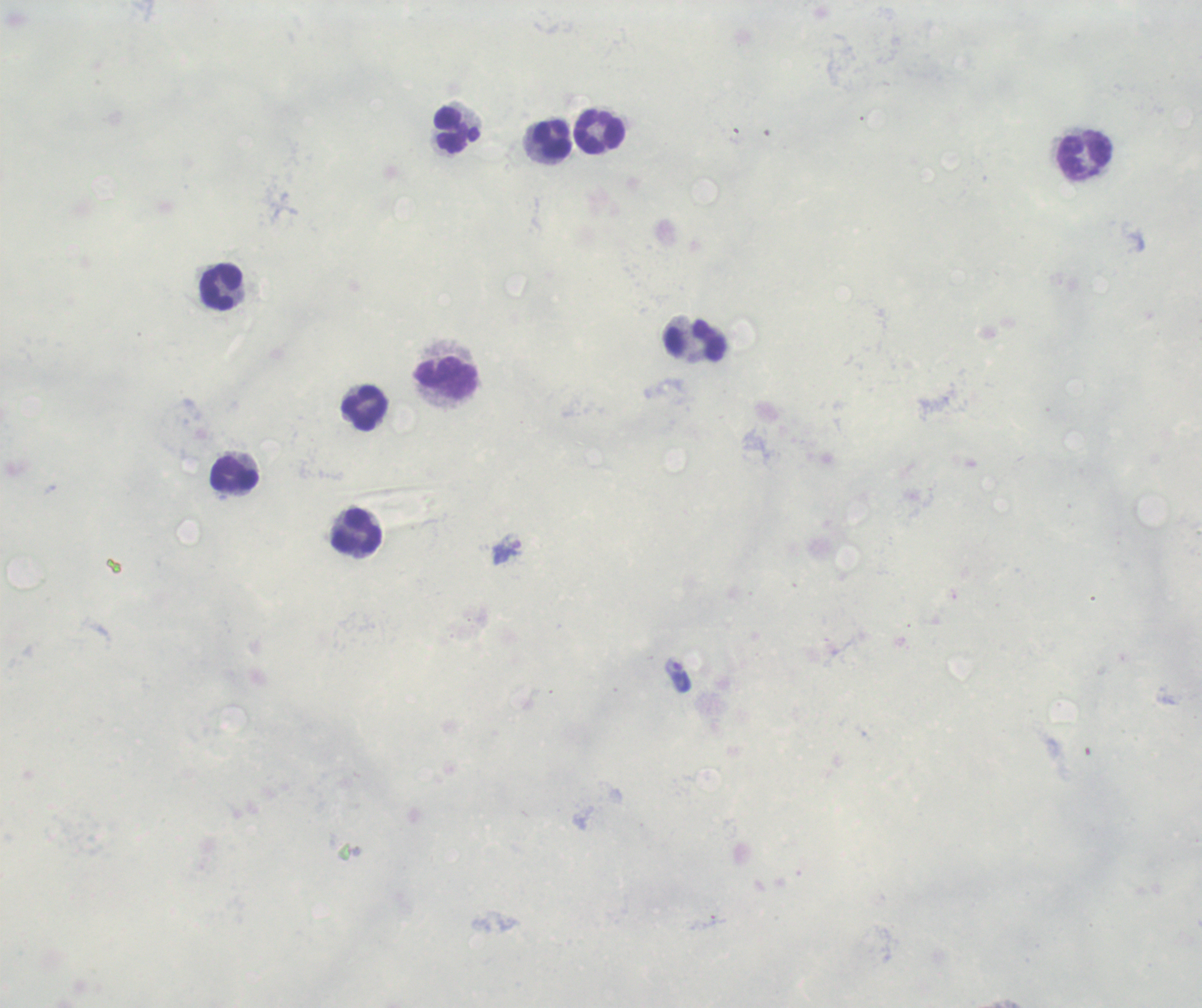

Approximate centers as (x, y) in pixels.
Summary:
  - Trophozoite locations: (506, 552), (678, 675)
  - Leukocyte locations: (456, 129), (599, 131), (552, 139), (1083, 157), (220, 287), (696, 341), (446, 378), (364, 409), (234, 475), (357, 533)
  - Result: Plasmodium parasites detected
  - Stain: Romanowsky
  - Preparation: thick blood smear
  - Context: previously used in a real diagnosis
  - Background quality: unsatisfactory
  - Image size: 1202×1008 pixels
  - Magnification: 100x
  - Field of view: one from this slide